State which cell type is depicted.
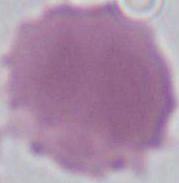

This is an erythrocyte.

{
  "modality": "micrograph",
  "magnification": "1000x"
}